Outline each blood parasite and name the species.
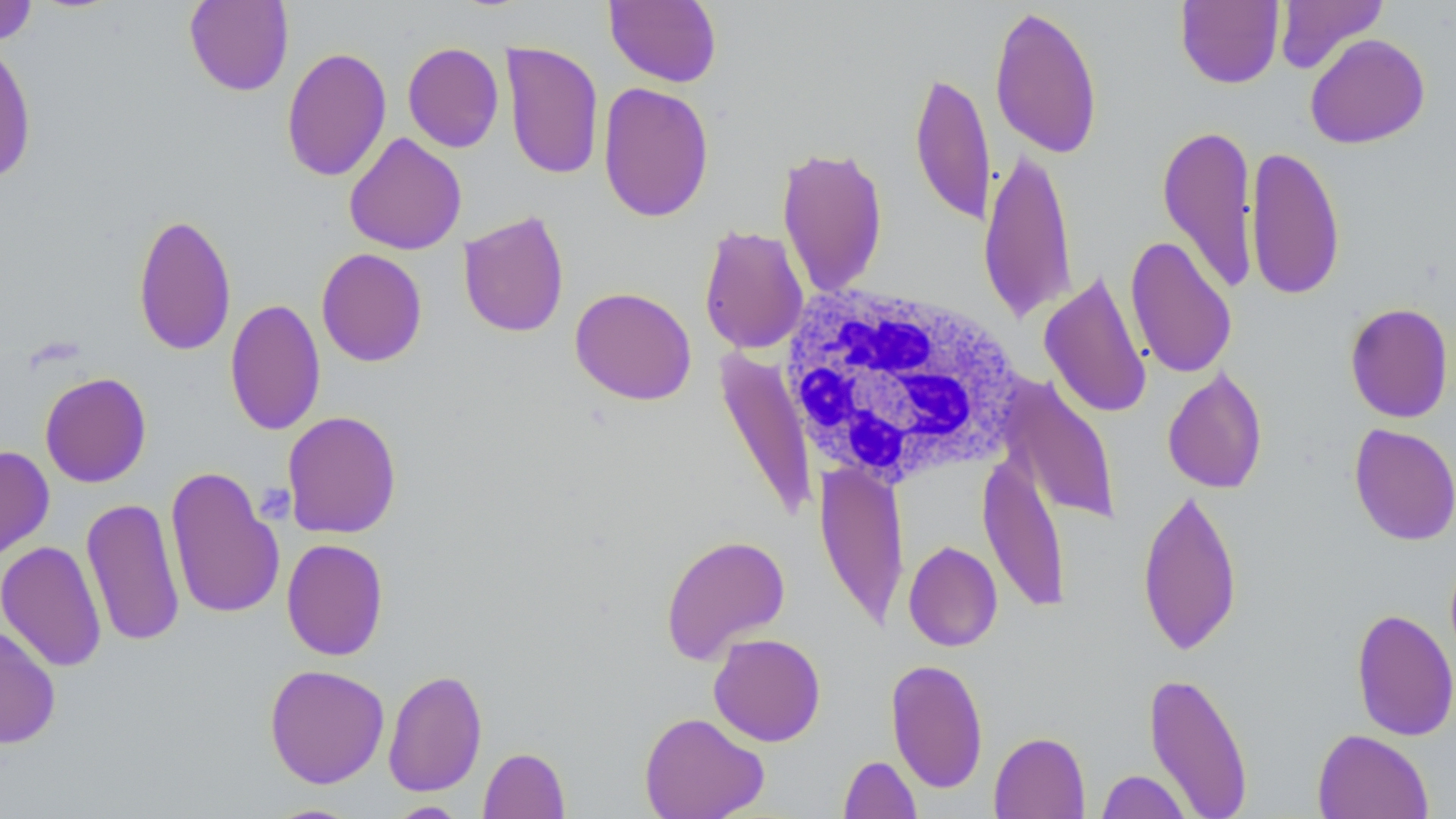

No blood parasites seen.

Summary:
  - Coordinate format: approximate bounding boxes as named x1/y1/x2/y2 corners in pixels
  - White blood cell locations: (x1=781, y1=282, x2=1026, y2=490)
  - Platelet locations: (x1=255, y1=482, x2=296, y2=523)
  - Uninfected red blood cell locations: (x1=184, y1=0, x2=294, y2=96), (x1=1175, y1=0, x2=1285, y2=89), (x1=1274, y1=0, x2=1388, y2=75), (x1=0, y1=1, x2=39, y2=47), (x1=604, y1=1, x2=722, y2=87), (x1=988, y1=4, x2=1104, y2=159), (x1=1305, y1=33, x2=1430, y2=149), (x1=0, y1=40, x2=38, y2=185), (x1=500, y1=41, x2=604, y2=181), (x1=403, y1=42, x2=504, y2=153), (x1=281, y1=46, x2=392, y2=182), (x1=909, y1=69, x2=995, y2=226), (x1=598, y1=82, x2=714, y2=223), (x1=1157, y1=123, x2=1259, y2=294), (x1=344, y1=133, x2=467, y2=255), (x1=980, y1=144, x2=1078, y2=325), (x1=777, y1=145, x2=889, y2=298), (x1=1245, y1=145, x2=1346, y2=301), (x1=458, y1=210, x2=570, y2=339), (x1=132, y1=212, x2=237, y2=356), (x1=698, y1=225, x2=810, y2=354), (x1=1124, y1=235, x2=1238, y2=379), (x1=316, y1=248, x2=428, y2=367), (x1=1040, y1=270, x2=1153, y2=420), (x1=569, y1=286, x2=697, y2=405), (x1=224, y1=298, x2=326, y2=436), (x1=1344, y1=302, x2=1454, y2=424), (x1=714, y1=350, x2=818, y2=521), (x1=1162, y1=368, x2=1269, y2=494), (x1=39, y1=372, x2=152, y2=488), (x1=1000, y1=375, x2=1122, y2=526), (x1=281, y1=410, x2=402, y2=539), (x1=1349, y1=424, x2=1456, y2=546), (x1=0, y1=445, x2=55, y2=562), (x1=978, y1=453, x2=1072, y2=614), (x1=814, y1=460, x2=909, y2=631), (x1=164, y1=466, x2=284, y2=621), (x1=1137, y1=486, x2=1243, y2=656), (x1=81, y1=496, x2=185, y2=648), (x1=660, y1=533, x2=791, y2=664), (x1=281, y1=539, x2=389, y2=661), (x1=1, y1=540, x2=107, y2=672), (x1=903, y1=540, x2=1003, y2=652), (x1=1351, y1=608, x2=1456, y2=741), (x1=0, y1=624, x2=60, y2=750), (x1=708, y1=633, x2=826, y2=746), (x1=886, y1=658, x2=988, y2=793), (x1=264, y1=664, x2=390, y2=789), (x1=383, y1=668, x2=488, y2=797), (x1=1144, y1=670, x2=1254, y2=818), (x1=639, y1=711, x2=769, y2=819), (x1=1312, y1=729, x2=1433, y2=819), (x1=989, y1=731, x2=1090, y2=819), (x1=479, y1=747, x2=570, y2=819), (x1=838, y1=754, x2=922, y2=818), (x1=1096, y1=769, x2=1192, y2=819), (x1=388, y1=801, x2=468, y2=818), (x1=261, y1=802, x2=366, y2=818)
  - Slide-level diagnosis: no evidence of blood parasites
  - Magnification: 1000x
  - Stain: May-Grünwald-Giemsa
  - Modality: optical microscopy
  - Field of view: one of a larger specimen
  - Image size: 1456×819 pixels
  - Preparation: thin blood smear